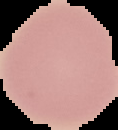

image type = cell region segmented out of the field of view; surrounding area masked to black
malaria status = uninfected
image size = 118×130 pixels
preparation = thin blood film